Outline each Babesia divergens-infected red blood cell.
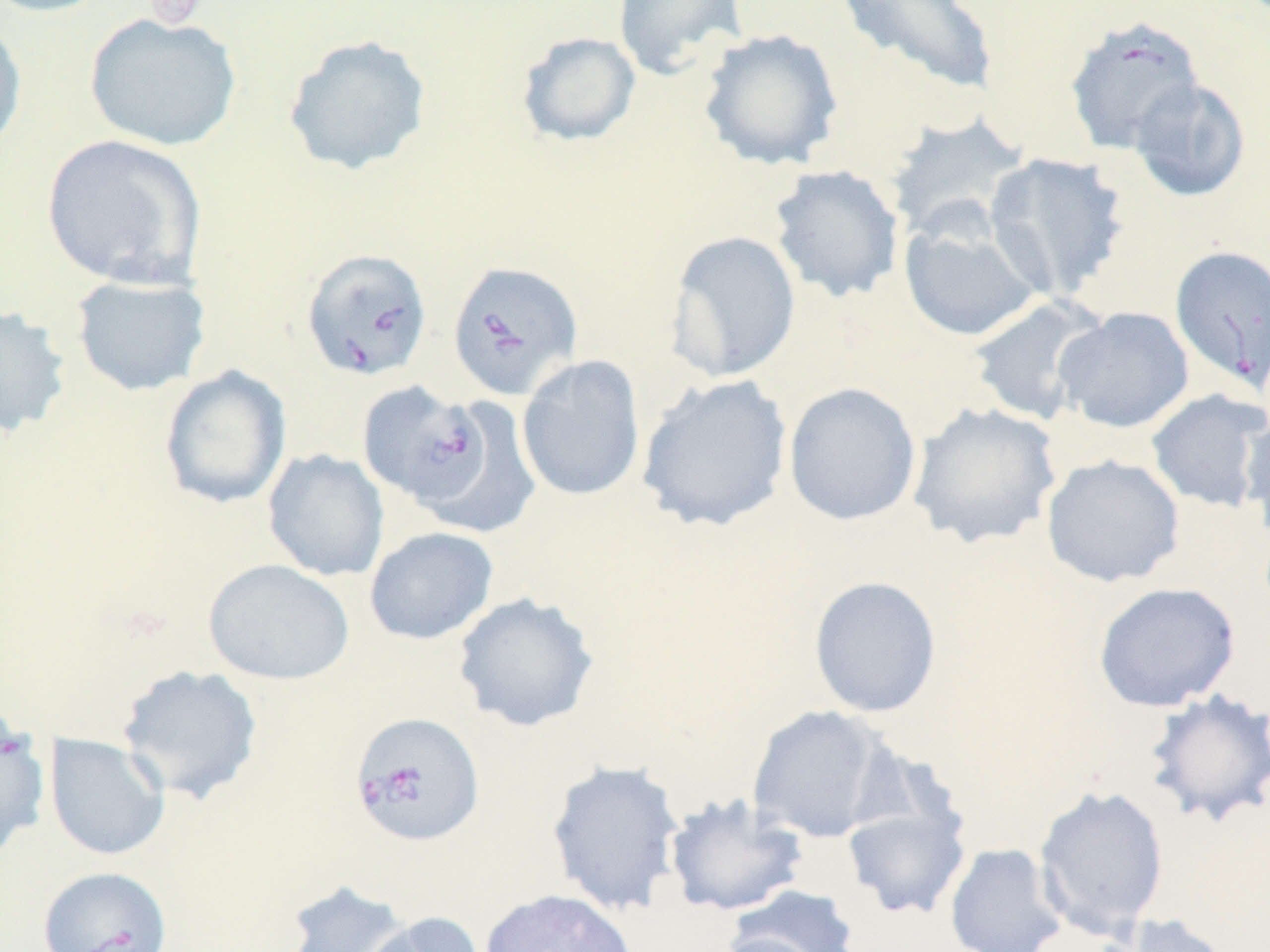
Approximate bounding boxes as [x1, y1, x2, y2] in pixels.
Babesia divergens-infected red blood cells: [1064, 15, 1205, 155], [1169, 245, 1270, 392], [301, 247, 433, 381], [446, 260, 582, 401], [357, 381, 490, 508], [349, 710, 485, 848], [37, 866, 173, 952].

{
  "slide_level_diagnosis": "Babesia divergens",
  "uninfected_red_blood_cell_locations": "approximate bounding boxes as [x1, y1, x2, y2] in pixels: [0, 0, 113, 18], [612, 0, 748, 80], [835, 0, 1000, 100], [0, 12, 28, 157], [84, 12, 242, 151], [697, 28, 845, 171], [516, 31, 641, 147], [282, 34, 433, 177], [1128, 77, 1251, 202], [882, 112, 1031, 243], [40, 134, 207, 289], [983, 151, 1131, 303], [768, 164, 905, 303], [899, 216, 1043, 342], [666, 230, 801, 383], [68, 273, 212, 396], [968, 296, 1108, 425], [0, 304, 73, 441], [1053, 306, 1194, 434], [516, 354, 646, 501], [159, 365, 292, 510], [636, 374, 793, 532], [783, 382, 923, 526], [1146, 388, 1270, 512], [429, 396, 542, 540], [907, 401, 1063, 550], [1239, 410, 1270, 543], [262, 449, 389, 582], [1040, 454, 1185, 588], [364, 526, 499, 645], [202, 558, 355, 685], [808, 575, 942, 718], [1092, 581, 1240, 712], [452, 591, 600, 733], [115, 664, 264, 805], [1142, 688, 1270, 829], [746, 705, 897, 843], [0, 725, 50, 860], [43, 733, 171, 862], [545, 759, 686, 916], [1033, 784, 1170, 939], [663, 793, 810, 917], [841, 796, 971, 919], [944, 842, 1068, 952], [280, 878, 419, 952], [725, 884, 861, 952], [479, 888, 638, 952], [360, 911, 486, 952], [1094, 914, 1236, 952], [711, 932, 832, 952]",
  "field_of_view": "single",
  "stain": "May-Grünwald-Giemsa",
  "image_size": "1270×952 pixels",
  "platelet_locations": "approximate bounding boxes as [x1, y1, x2, y2] in pixels: [144, 0, 209, 30]",
  "preparation": "thin blood smear",
  "modality": "optical microscopy",
  "magnification": "1000x"
}